Identify the parasite.
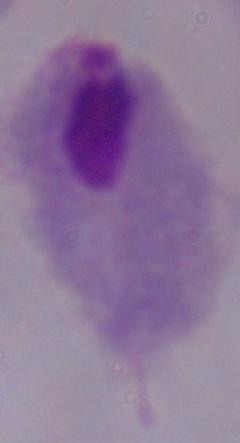
This is a trichomonad.

Summary:
  - Magnification: 1000x
  - Modality: micrograph